Describe the morphology of the erythrocytes.
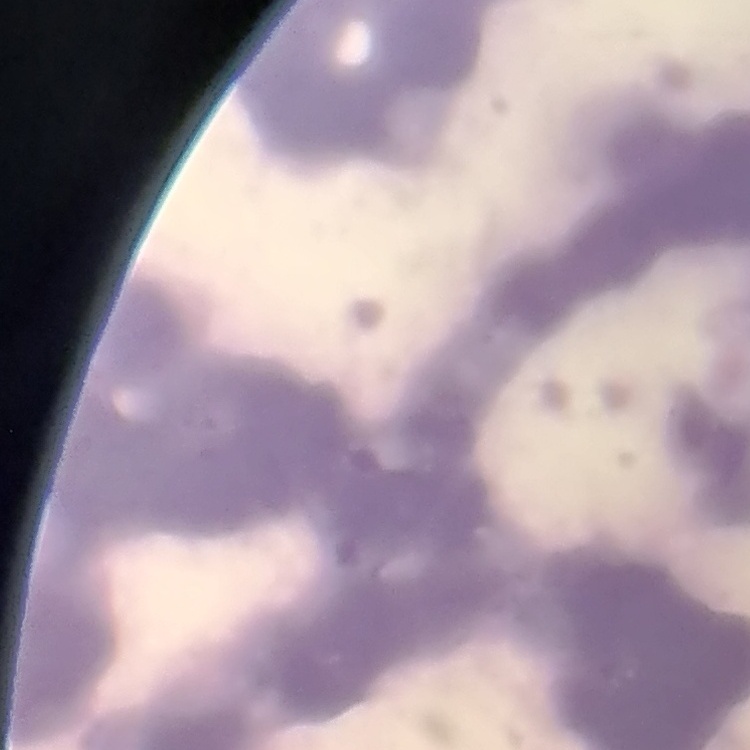
Rouleaux formation.

Summary:
  - Preparation: thin blood film
  - Image type: square crop of a larger photomicrograph
  - Stain: Field's or Giemsa